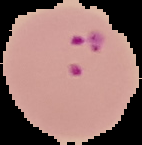
image_type: segmented cell region on a black background
malaria_status: parasitized
image_size: 142×145 pixels
preparation: thin blood film